Assess this cell for malaria.
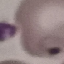
It is parasitized.

{
  "capture": "smartphone through the microscope eyepiece",
  "stain": "Giemsa",
  "preparation": "thin smear",
  "image_type": "automatically extracted cell patch, resized to 64 × 64 pixels"
}